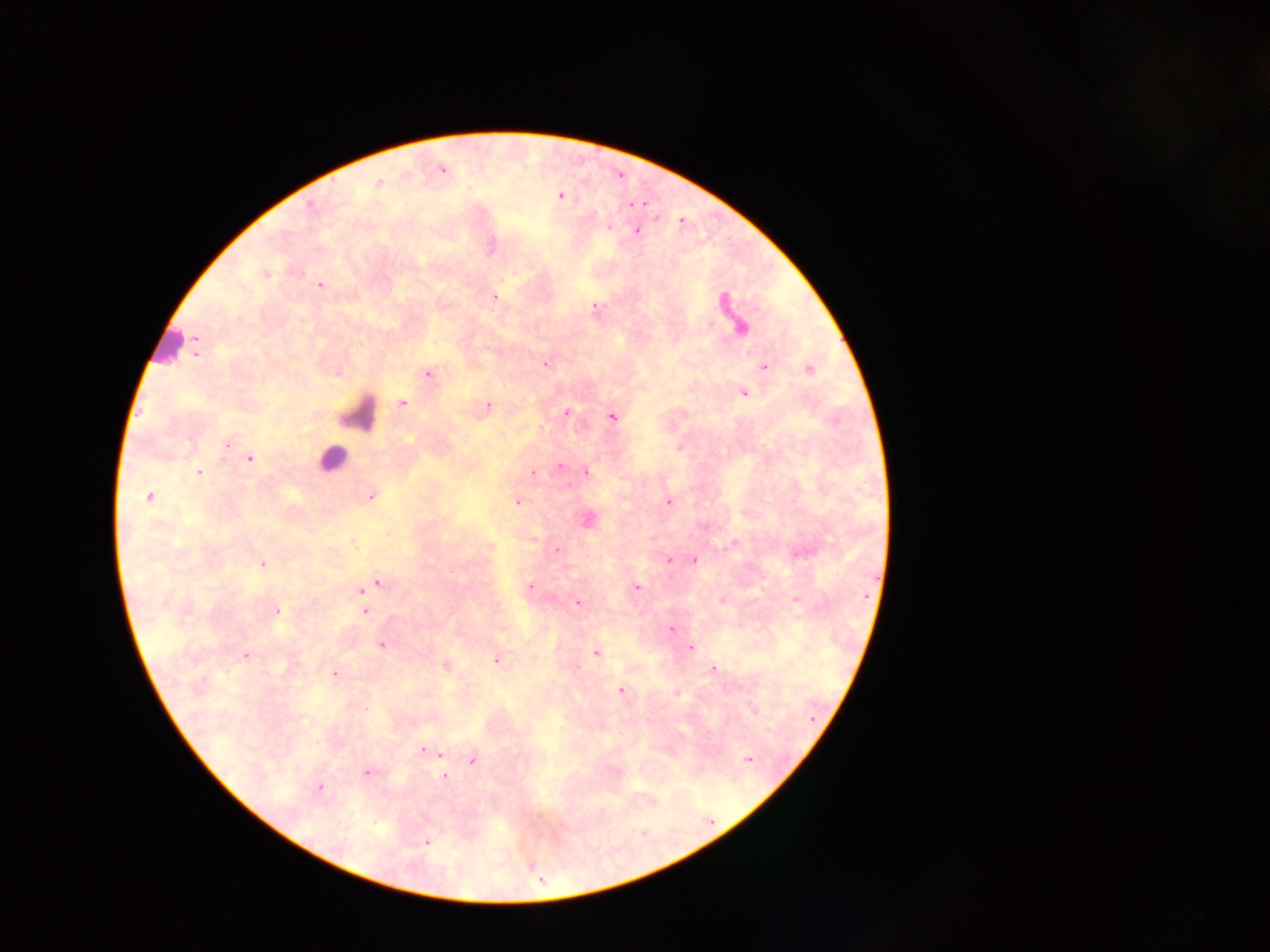

Approximate centers as {x, y} in pixels.
Summary:
  - Leukocyte locations: {166, 343}, {356, 413}, {345, 447}, {330, 459}
  - Plasmodium parasite locations: {441, 169}, {378, 184}, {560, 196}, {608, 227}, {636, 230}, {491, 246}, {266, 273}, {320, 284}, {494, 297}, {594, 309}, {740, 327}, {195, 338}, {195, 349}, {545, 363}, {764, 366}, {808, 368}, {338, 372}, {427, 374}, {742, 391}, {402, 402}, {488, 406}, {567, 413}, {612, 416}, {227, 444}, {249, 458}, {560, 466}, {586, 471}, {199, 472}, {533, 472}, {371, 495}, {149, 496}, {517, 501}, {668, 502}, {587, 519}, {534, 539}, {351, 541}, {734, 544}, {558, 550}, {668, 559}, {694, 560}, {262, 563}, {377, 582}, {370, 586}, {529, 587}, {637, 587}, {361, 590}, {722, 599}, {796, 599}, {576, 602}, {275, 611}, {365, 611}, {670, 629}, {382, 644}, {689, 647}, {595, 652}, {245, 655}, {497, 660}, {446, 665}, {712, 670}, {334, 673}, {621, 691}, {677, 693}, {753, 708}, {423, 750}, {430, 751}, {439, 753}, {748, 758}, {473, 759}, {366, 772}, {445, 775}, {319, 787}, {426, 842}
  - Image size: 1270×952 pixels
  - Field of view: single
  - Country: Ghana
  - Preparation: thick blood smear
  - Capture: mobile-phone photograph through a microscope